Identify the parasite.
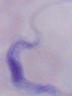

This is a trypanosome.

magnification: 1000x
modality: photomicrograph